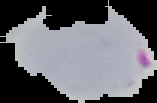

Image is 157×103 pixels. Cell region segmented out of the field of view; the surrounding area is masked to black. Result: malaria parasites identified. From a thin blood film.